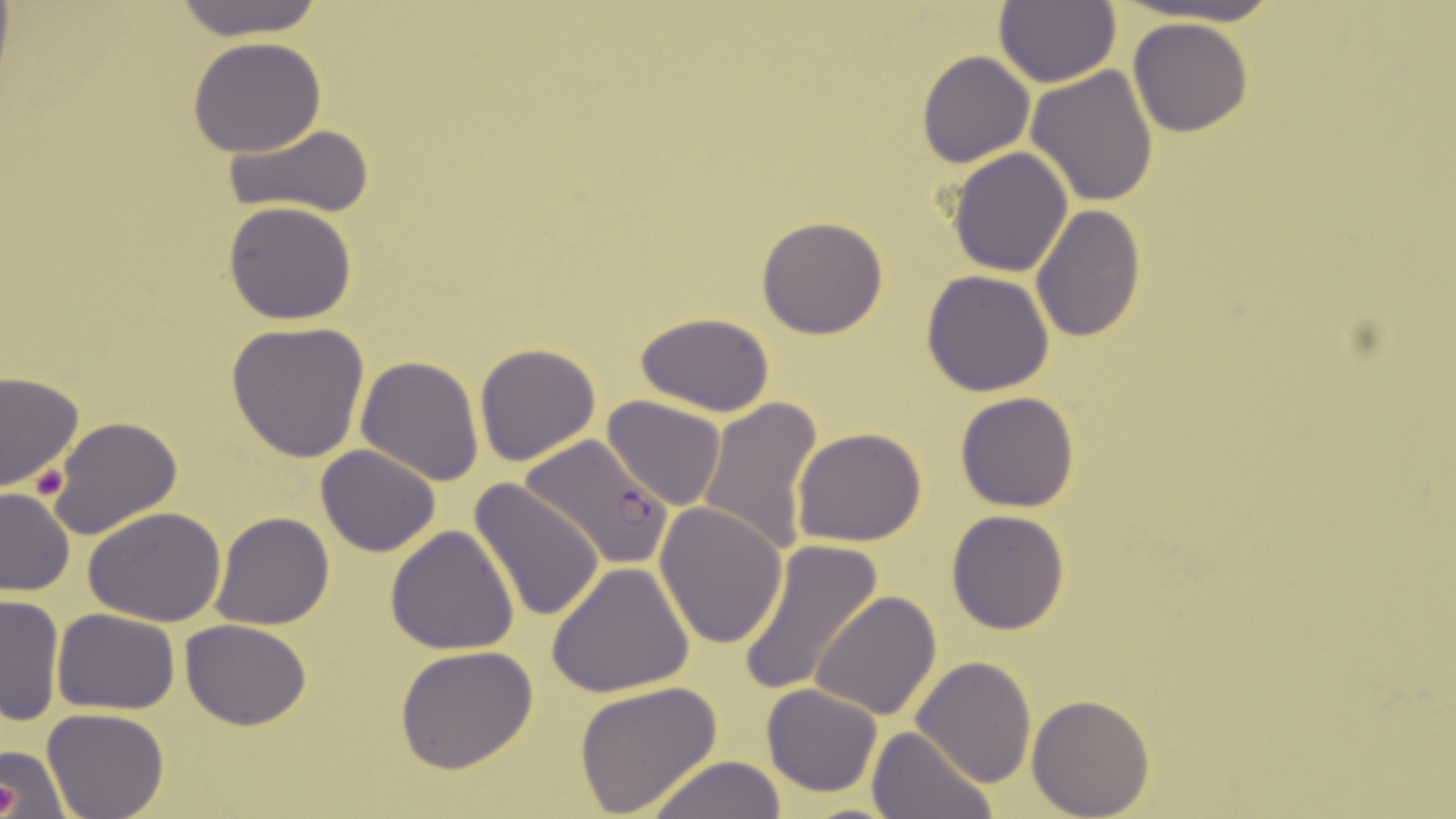
slide-level diagnosis = Plasmodium falciparum
modality = optical microscopy
uninfected red blood cell locations = approximate bounding boxes as (x1,y1)-(x2,y2) corner pairs in pixels: (167,0)-(329,40), (995,0)-(1121,89), (1128,17)-(1254,137), (186,37)-(328,157), (917,51)-(1033,166), (1026,65)-(1159,207), (223,122)-(379,219), (948,148)-(1074,278), (222,200)-(358,324), (1030,203)-(1145,342), (756,215)-(889,339), (921,269)-(1055,395), (636,314)-(776,417), (225,319)-(371,462), (475,341)-(600,467), (356,354)-(486,485), (0,370)-(83,492), (955,391)-(1081,513), (604,395)-(727,511), (697,396)-(824,559), (48,417)-(182,539), (793,427)-(926,547), (316,445)-(440,558), (468,478)-(606,623), (0,485)-(74,595), (655,502)-(789,649), (83,507)-(227,626), (946,509)-(1070,634), (210,511)-(335,629), (385,526)-(520,655), (738,540)-(883,696), (546,563)-(694,696), (810,591)-(942,720), (1,592)-(65,726), (53,609)-(180,713), (181,618)-(312,730), (395,645)-(539,775), (912,656)-(1036,789), (573,679)-(721,818), (761,683)-(882,797), (1026,695)-(1154,818), (42,709)-(169,819), (867,726)-(996,819), (0,743)-(71,819), (642,756)-(792,818)
preparation = thin blood smear
magnification = 1000x
Plasmodium falciparum-infected red blood cell locations = approximate bounding boxes as (x1,y1)-(x2,y2) corner pairs in pixels: (523,433)-(671,569)
image size = 1456×819 pixels
platelet locations = approximate bounding boxes as (x1,y1)-(x2,y2) corner pairs in pixels: (31,462)-(70,503), (0,783)-(21,813)
field of view = single
stain = May-Grünwald-Giemsa